Identify the parasite.
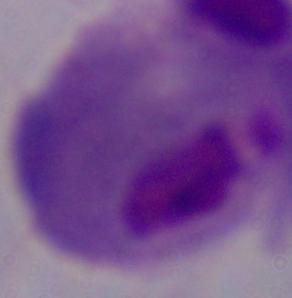
A trichomonad.

magnification: 1000x
modality: photomicrograph